Locate every P. falciparum parasite and give its life-cycle stage, and locate every leukocyte and any debris.
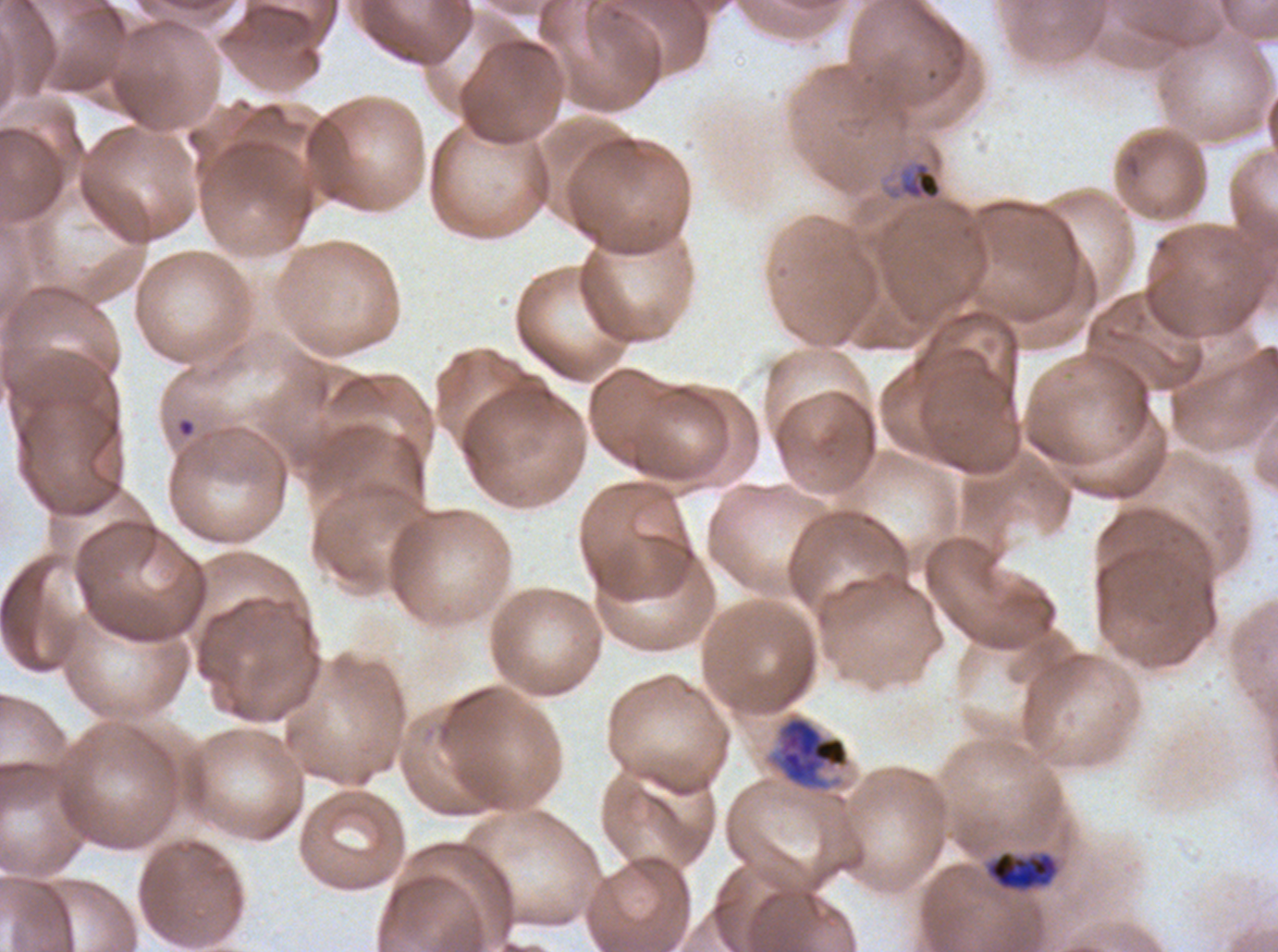
Approximate bounding rectangles given as corner coordinates in pixels from the top-left.
Early schizonts: (x1=763, y1=710, x2=853, y2=795), (x1=986, y1=849, x2=1059, y2=892).
Debris: (x1=890, y1=160, x2=943, y2=201).
No rings, late-ring/early-trophozoite forms, mid trophozoites, late trophozoites, late schizonts, segmenters, gametocytes, or leukocytes observed.

image size = 1278×952 pixels
stain = Giemsa
field of view = one sub-image of a larger composite
preparation = thin blood film
specimen = P. falciparum from a patient in The Gambia, cultured ex vivo for 24 to 48 hours